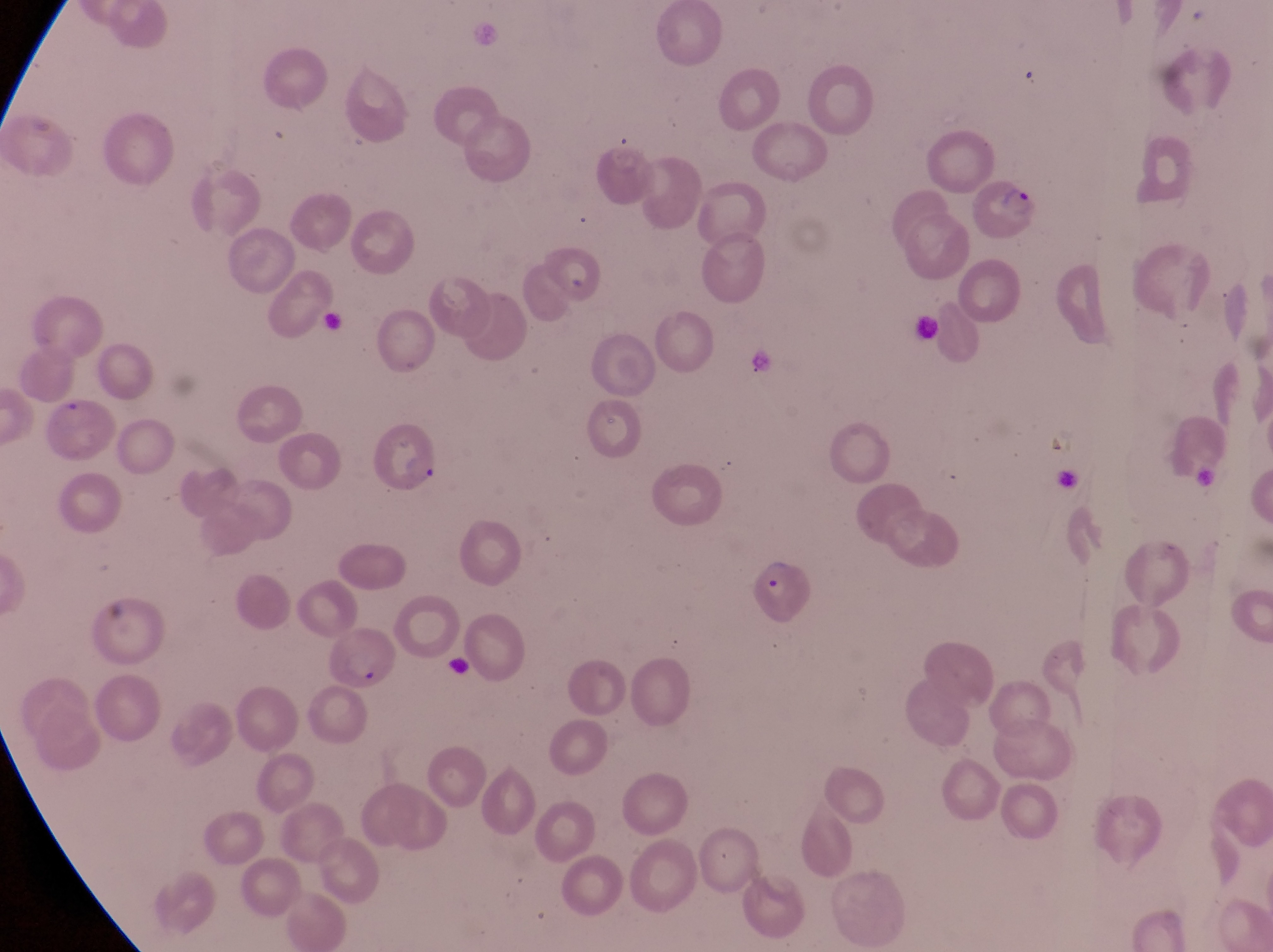

Approximate bounding boxes as {left, top, right, bottom} in pixels.
Summary:
  - Parasitised red blood cell locations: {969, 175, 1041, 235}, {534, 244, 597, 302}, {40, 390, 115, 462}, {369, 415, 443, 497}, {741, 547, 815, 640}, {319, 626, 397, 689}
  - Country: Uganda
  - Preparation: thin blood film
  - Capture: smartphone photograph through the eyepiece of an Olympus CX-23 microscope
  - Field of view: single
  - Image size: 1273×952 pixels
  - Magnification: 1000x